Comment on the morphology of the red blood cells.
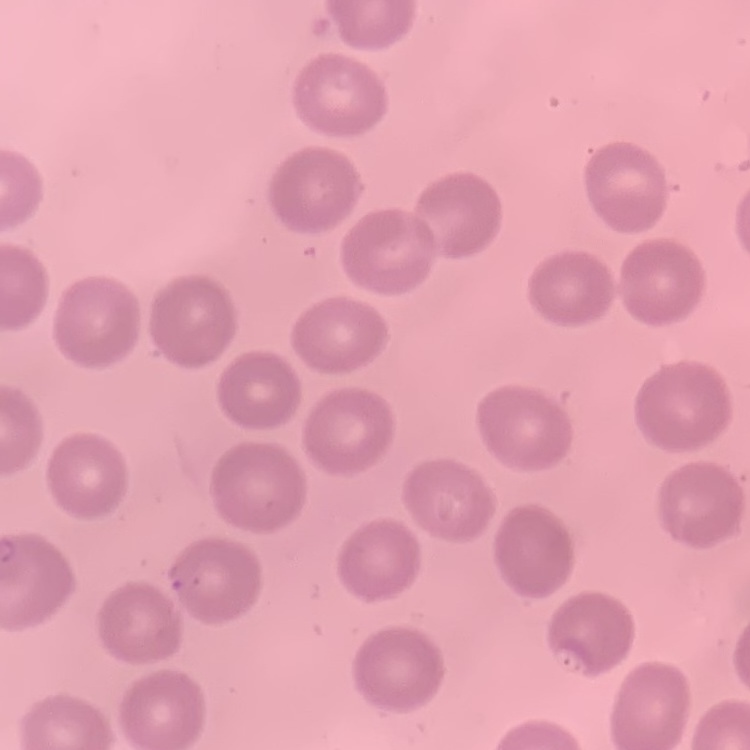
They show no rouleaux formation.

Stained with either Field's or Giemsa. One tile cut from a larger photomicrograph. Thin peripheral smear.